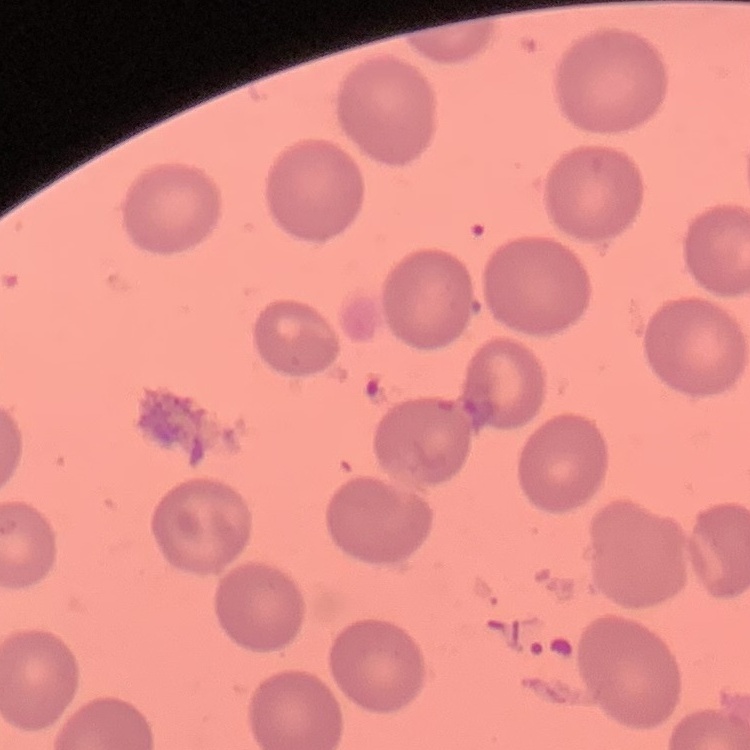
erythrocyte morphology = no rouleaux formation
stain = Field's or Giemsa
preparation = thin peripheral smear
image type = one tile cut from a larger photomicrograph